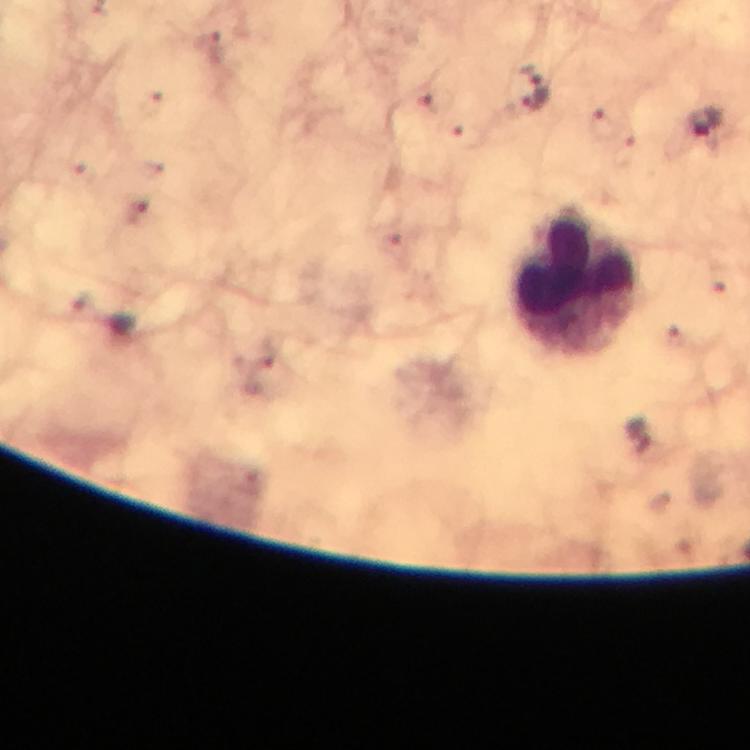
stain: Giemsa
magnification: 100x
image_size: 750×750 pixels
leukocyte_locations: 'approximate centers as [x, y] in pixels: [573, 282]'
malaria_parasite_locations: 'approximate centers as [x, y] in pixels: [532, 89], [704, 125]'
capture: smartphone mounted on the microscope
context: from a diagnostic examination for malaria
immersion_oil: used
preparation: thick blood smear
cropped_from: a single field of view